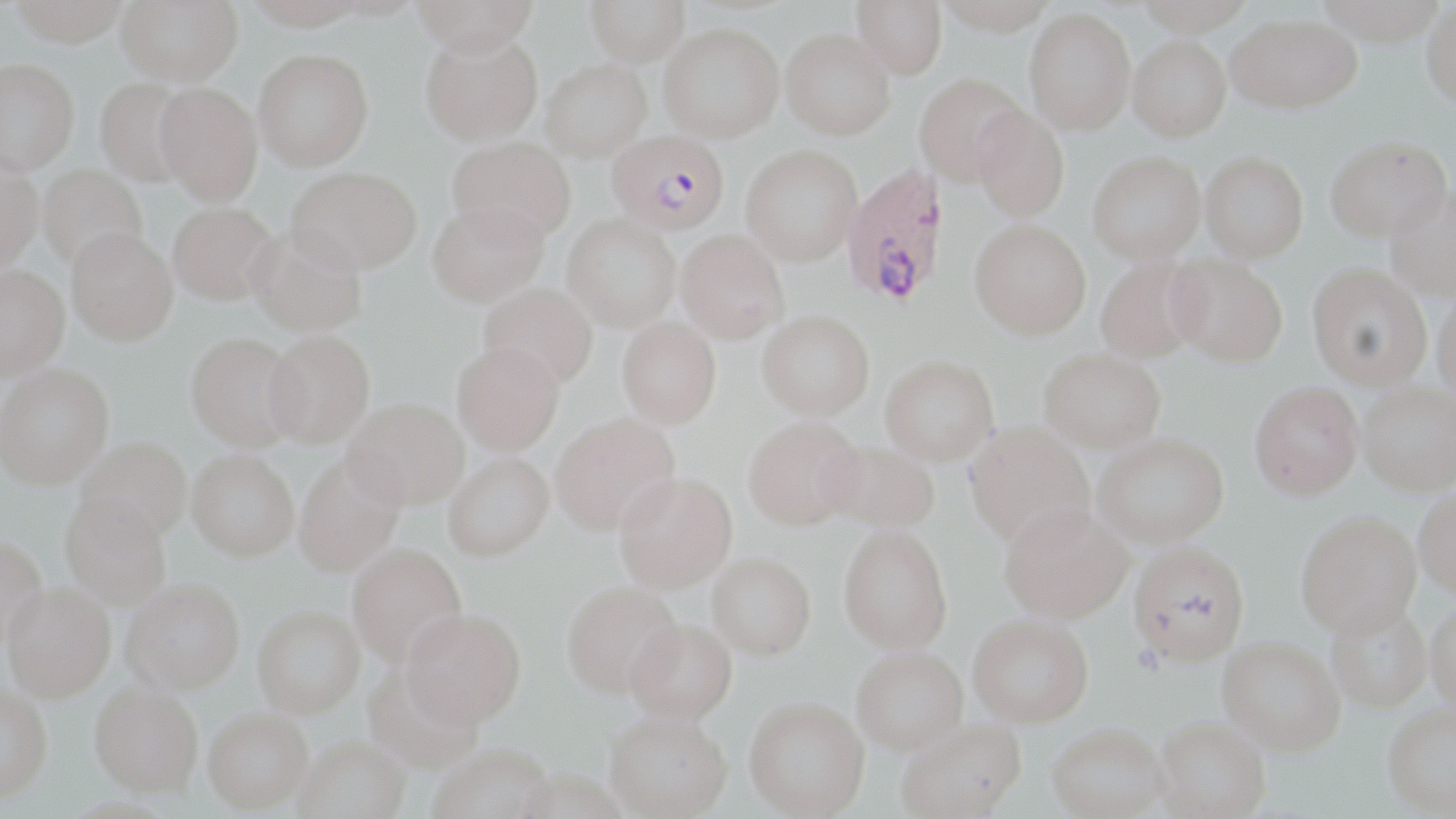
Approximate bounding boxes as named x1/y1/x2/y2 corners in pixels. Uninfected red blood cell locations: (x1=9, y1=0, x2=130, y2=48), (x1=115, y1=0, x2=243, y2=86), (x1=243, y1=0, x2=370, y2=29), (x1=412, y1=0, x2=538, y2=57), (x1=586, y1=0, x2=690, y2=66), (x1=852, y1=0, x2=947, y2=80), (x1=935, y1=0, x2=1059, y2=35), (x1=1421, y1=3, x2=1456, y2=114), (x1=1024, y1=6, x2=1136, y2=135), (x1=1226, y1=13, x2=1361, y2=113), (x1=659, y1=24, x2=784, y2=142), (x1=420, y1=28, x2=543, y2=146), (x1=781, y1=29, x2=896, y2=140), (x1=1128, y1=36, x2=1231, y2=141), (x1=253, y1=49, x2=373, y2=171), (x1=0, y1=58, x2=79, y2=173), (x1=540, y1=59, x2=652, y2=162), (x1=915, y1=72, x2=1028, y2=186), (x1=94, y1=78, x2=196, y2=188), (x1=155, y1=83, x2=263, y2=206), (x1=972, y1=104, x2=1070, y2=222), (x1=448, y1=136, x2=576, y2=243), (x1=1326, y1=141, x2=1452, y2=247), (x1=740, y1=144, x2=862, y2=266), (x1=1088, y1=150, x2=1206, y2=264), (x1=1201, y1=151, x2=1308, y2=262), (x1=0, y1=160, x2=43, y2=271), (x1=38, y1=164, x2=147, y2=270), (x1=287, y1=166, x2=421, y2=273), (x1=1386, y1=188, x2=1456, y2=303), (x1=427, y1=200, x2=549, y2=307), (x1=167, y1=202, x2=279, y2=305), (x1=562, y1=214, x2=681, y2=331), (x1=969, y1=219, x2=1091, y2=339), (x1=246, y1=226, x2=368, y2=337), (x1=66, y1=227, x2=178, y2=346), (x1=676, y1=230, x2=788, y2=343), (x1=1166, y1=256, x2=1286, y2=368), (x1=1096, y1=257, x2=1207, y2=363), (x1=0, y1=264, x2=69, y2=379), (x1=1307, y1=268, x2=1431, y2=393), (x1=478, y1=283, x2=598, y2=390), (x1=1432, y1=295, x2=1456, y2=405), (x1=757, y1=309, x2=874, y2=420), (x1=617, y1=317, x2=721, y2=428), (x1=265, y1=330, x2=375, y2=447), (x1=186, y1=332, x2=304, y2=451), (x1=451, y1=341, x2=564, y2=456), (x1=1039, y1=348, x2=1166, y2=452), (x1=880, y1=355, x2=999, y2=465), (x1=0, y1=363, x2=114, y2=489), (x1=1249, y1=386, x2=1363, y2=505), (x1=1358, y1=388, x2=1456, y2=499), (x1=343, y1=398, x2=469, y2=509), (x1=549, y1=413, x2=680, y2=535), (x1=743, y1=415, x2=864, y2=530), (x1=965, y1=423, x2=1095, y2=547), (x1=1093, y1=433, x2=1228, y2=548), (x1=75, y1=437, x2=192, y2=541), (x1=820, y1=440, x2=939, y2=533), (x1=187, y1=449, x2=299, y2=560), (x1=293, y1=452, x2=404, y2=578), (x1=443, y1=452, x2=553, y2=561), (x1=613, y1=471, x2=737, y2=593), (x1=1414, y1=493, x2=1456, y2=606), (x1=60, y1=495, x2=172, y2=610), (x1=999, y1=502, x2=1132, y2=624), (x1=1297, y1=516, x2=1422, y2=645), (x1=839, y1=524, x2=953, y2=653), (x1=0, y1=535, x2=47, y2=650), (x1=347, y1=543, x2=468, y2=668), (x1=1128, y1=545, x2=1250, y2=671), (x1=707, y1=552, x2=816, y2=659), (x1=121, y1=578, x2=245, y2=695), (x1=561, y1=581, x2=684, y2=698), (x1=3, y1=584, x2=116, y2=704), (x1=1426, y1=605, x2=1456, y2=722), (x1=252, y1=606, x2=365, y2=720), (x1=401, y1=608, x2=526, y2=731), (x1=1326, y1=608, x2=1433, y2=716), (x1=968, y1=617, x2=1093, y2=731), (x1=624, y1=621, x2=737, y2=730), (x1=1217, y1=641, x2=1344, y2=762), (x1=851, y1=651, x2=968, y2=761), (x1=363, y1=667, x2=482, y2=776), (x1=89, y1=687, x2=203, y2=802), (x1=0, y1=688, x2=53, y2=808), (x1=743, y1=702, x2=869, y2=819), (x1=1383, y1=708, x2=1456, y2=818), (x1=203, y1=713, x2=314, y2=817), (x1=604, y1=718, x2=732, y2=819), (x1=1153, y1=722, x2=1271, y2=819), (x1=896, y1=724, x2=1027, y2=819), (x1=1047, y1=730, x2=1169, y2=819), (x1=294, y1=742, x2=410, y2=819), (x1=429, y1=748, x2=555, y2=819). Plasmodium falciparum-infected red blood cell locations: (x1=606, y1=129, x2=729, y2=233), (x1=842, y1=163, x2=950, y2=308). Slide-level diagnosis: Plasmodium falciparum. Optical microscopy. Captured at 1000x magnification. May-Grünwald-Giemsa-stained preparation. Image is 1456×819 pixels. Thin blood smear. One field of a larger specimen.